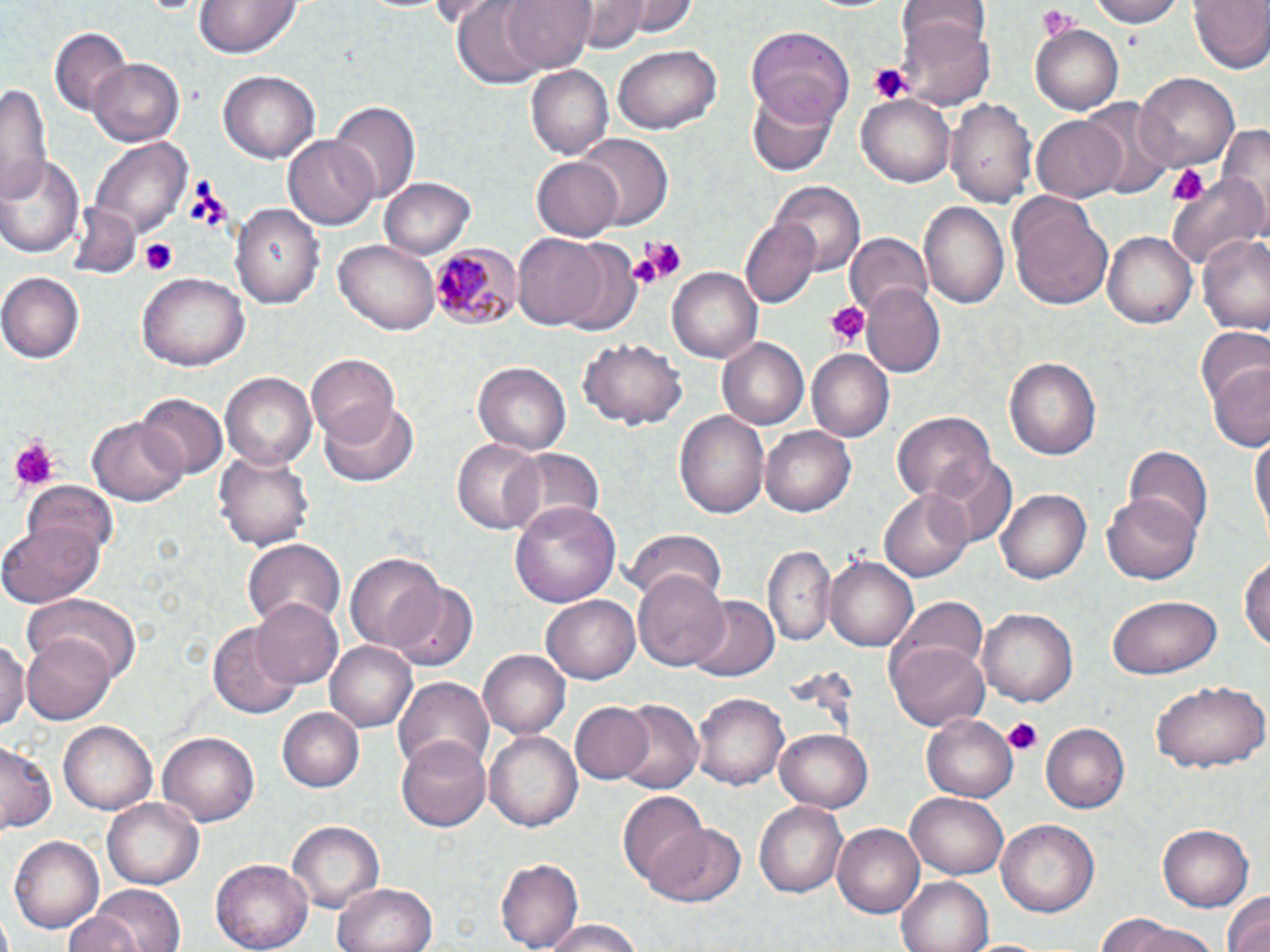
Approximate bounding boxes as (x1,y1)-(x2,y2) corner pairs in pixels. Plasmodium malariae-infected red blood cell locations: (428,240)-(520,327). Platelet locations: (1036,6)-(1081,39), (867,61)-(913,104), (1166,163)-(1208,206), (139,237)-(177,275), (632,240)-(689,283), (625,248)-(668,289), (825,302)-(866,347), (8,435)-(58,490), (1002,716)-(1044,756). Uninfected red blood cell locations: (451,0)-(552,87), (502,0)-(594,73), (575,0)-(661,50), (620,0)-(698,36), (1086,0)-(1187,26), (1188,0)-(1269,75), (195,1)-(300,60), (900,1)-(988,57), (899,19)-(993,106), (1031,22)-(1126,113), (747,24)-(854,123), (50,27)-(131,115), (611,45)-(721,135), (89,58)-(183,147), (526,67)-(613,159), (220,69)-(321,163), (1134,72)-(1240,173), (1,79)-(53,204), (745,89)-(837,176), (1079,96)-(1175,197), (948,97)-(1037,211), (858,98)-(955,186), (331,101)-(418,207), (1030,114)-(1127,203), (1217,120)-(1270,223), (286,134)-(381,230), (576,135)-(671,229), (89,136)-(191,237), (2,154)-(83,257), (531,156)-(624,242), (1167,166)-(1270,273), (379,176)-(477,259), (770,181)-(864,277), (1008,196)-(1114,311), (231,200)-(325,305), (919,202)-(1008,310), (68,204)-(141,278), (741,216)-(820,307), (1197,231)-(1270,335), (1103,232)-(1195,328), (514,234)-(609,331), (844,234)-(930,316), (334,236)-(441,334), (551,239)-(644,337), (669,266)-(761,363), (138,272)-(249,372), (2,273)-(84,364), (861,283)-(945,377), (1196,328)-(1270,415), (717,336)-(813,430), (579,338)-(688,430), (805,348)-(893,440), (306,352)-(400,442), (1006,357)-(1101,462), (1209,357)-(1270,453), (473,360)-(573,455), (221,371)-(318,471), (136,393)-(226,479), (321,401)-(419,487), (675,411)-(769,518), (892,411)-(993,505), (87,418)-(187,504), (761,425)-(855,516), (1250,428)-(1269,548), (452,441)-(542,532), (1121,444)-(1213,537), (215,446)-(314,553), (502,448)-(604,536), (931,455)-(1017,550), (22,479)-(120,558), (879,488)-(975,582), (995,489)-(1089,585), (1104,490)-(1201,582), (511,502)-(620,607), (2,519)-(102,605), (623,529)-(726,607), (243,539)-(345,629), (763,547)-(835,649), (345,549)-(446,654), (1239,550)-(1270,659), (826,555)-(919,652), (633,569)-(729,673), (388,582)-(479,674), (24,592)-(145,689), (248,595)-(344,691), (543,595)-(641,685), (1107,595)-(1223,678), (689,597)-(778,683), (895,598)-(988,680), (978,607)-(1076,707), (209,620)-(302,718), (23,632)-(116,723), (0,637)-(27,731), (890,639)-(990,731), (326,641)-(417,733), (479,648)-(571,739), (391,675)-(494,779), (1151,679)-(1267,773), (692,692)-(788,791), (612,700)-(704,794), (567,701)-(655,785), (279,708)-(365,792), (923,710)-(1020,802), (59,720)-(159,814), (1041,723)-(1131,814), (484,729)-(583,831), (775,729)-(875,813), (159,732)-(259,826), (397,736)-(495,831), (0,743)-(56,832), (617,791)-(706,885), (906,792)-(1008,880), (104,798)-(202,889), (755,799)-(849,897), (995,820)-(1101,919), (290,821)-(383,915), (647,821)-(744,908), (833,822)-(925,919), (1157,824)-(1257,911), (9,835)-(104,935), (212,858)-(313,951), (497,859)-(583,949), (896,875)-(992,952), (332,881)-(438,952), (88,885)-(185,952), (1218,889)-(1270,952), (61,907)-(142,952), (1095,915)-(1184,950), (540,922)-(648,952), (1118,923)-(1221,952). Slide-level diagnosis: Plasmodium malariae. May-Grünwald-Giemsa stain. Thin blood smear. One field of a larger specimen. 1000x magnification. Image is 1270×952 pixels. Optical microscopy.